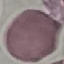

malaria status = uninfected
image type = automatically extracted cell patch, resized to 64 × 64 pixels
stain = Giemsa
capture = smartphone through the microscope eyepiece
preparation = thin smear